Classify this cell by malaria status.
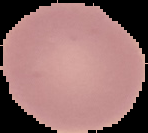

Uninfected.

image size = 148×133 pixels
image type = segmented cell region with the area outside set to black
preparation = thin blood film